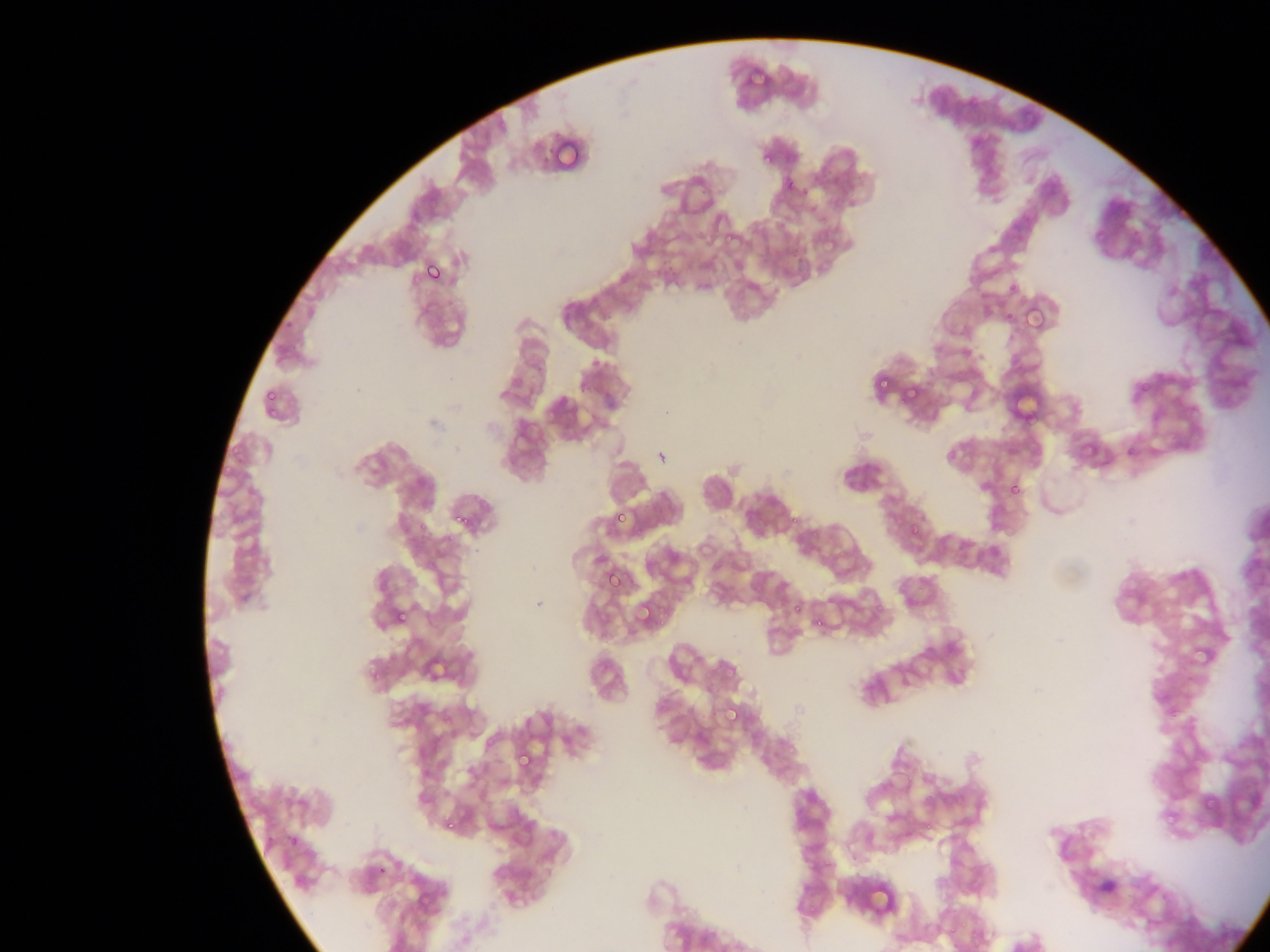 Approximate bounding boxes as {left, top, right, bottom} in pixels. Malaria parasite locations: {758, 153, 771, 162}, {781, 160, 795, 184}, {796, 187, 810, 201}, {719, 225, 736, 245}, {418, 254, 453, 293}, {422, 261, 445, 285}, {1019, 303, 1059, 340}, {872, 372, 898, 392}, {897, 379, 915, 403}, {262, 385, 282, 400}, {263, 408, 279, 418}, {230, 440, 247, 453}, {219, 468, 233, 477}, {1006, 480, 1024, 499}, {610, 503, 633, 529}, {451, 505, 479, 536}, {906, 523, 925, 547}, {601, 566, 626, 592}, {872, 594, 889, 611}, {786, 598, 805, 618}, {634, 600, 657, 628}, {392, 606, 411, 626}, {811, 615, 823, 632}, {427, 654, 454, 680}, {721, 703, 745, 730}, {513, 746, 536, 772}, {439, 809, 464, 834}, {441, 817, 456, 833}, {286, 832, 302, 850}, {863, 879, 889, 912}. Image is 1270×952 pixels. Collected in Ghana. Thin blood film. Mobile-phone photograph taken through the microscope. Single field of view.